Point out every malaria parasite.
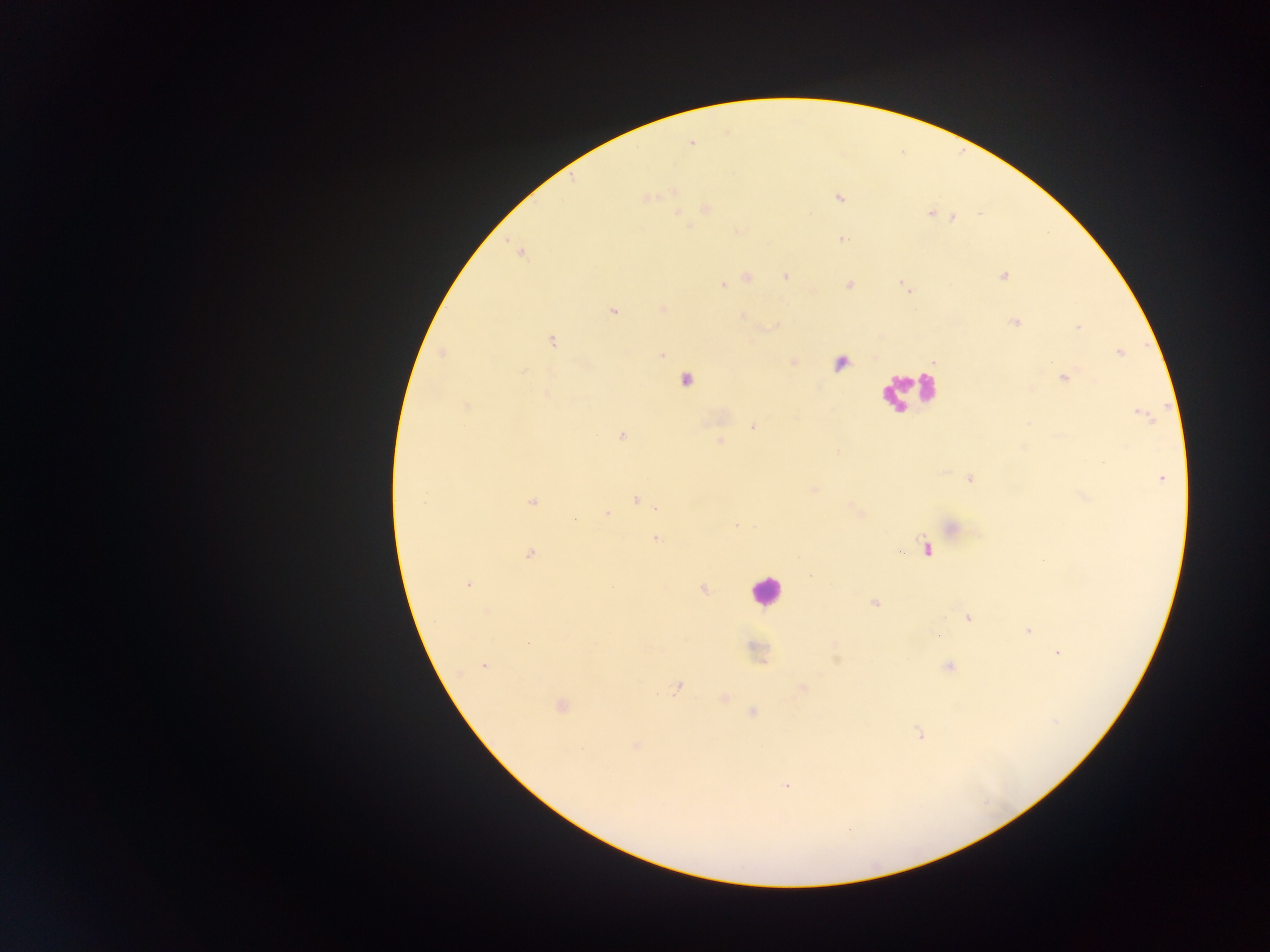
Approximate centers as [x, y] in pixels.
Malaria parasites: [691, 143], [646, 197], [839, 198], [705, 209], [930, 213], [678, 214], [954, 218], [842, 239], [519, 252], [1003, 276], [748, 277], [785, 277], [722, 285], [849, 285], [904, 286], [663, 309], [613, 310], [742, 317], [1014, 321], [1078, 326], [552, 341], [1119, 352], [442, 354], [661, 355], [1063, 377], [685, 380], [545, 394], [467, 405], [1143, 415], [753, 427], [621, 436], [720, 442], [971, 478], [1161, 478], [813, 490], [1085, 498], [636, 500], [532, 502], [656, 508], [860, 513], [606, 514], [736, 525], [952, 527], [655, 538], [926, 549], [529, 554], [468, 584], [703, 589], [875, 603], [487, 611], [969, 617], [1027, 630], [937, 634], [529, 643], [835, 645], [1058, 653], [484, 667], [949, 667], [677, 688], [803, 688], [724, 698], [560, 706], [752, 712], [919, 734], [637, 746], [787, 785].

Summary:
  - Leukocyte locations: [844, 362], [904, 389], [765, 591]
  - Capture: mobile-phone photograph through a microscope
  - Field of view: single
  - Image size: 1270×952 pixels
  - Country: Ghana
  - Preparation: thick blood smear